Classify this cell by malaria status.
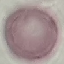
Uninfected.

image type = automatically extracted cell patch, resized to 64 × 64 pixels
capture = smartphone through the microscope eyepiece
preparation = thin blood film
stain = Giemsa